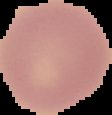
Summary:
  - Image size: 112×115 pixels
  - Result: no malaria parasites seen
  - Preparation: thin blood smear
  - Image type: segmented cell region on a black background